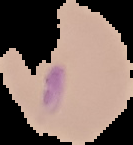
Result: Plasmodium parasites detected. Image is 133×145 pixels. The area outside the segmented cell region is set to black. From a thin blood film.